Report the malaria status of this cell.
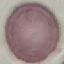
It is uninfected.

image type = automatically extracted cell patch, resized to 64 × 64 pixels
capture = smartphone camera at the microscope eyepiece
preparation = thin blood smear
stain = Giemsa